Comment on the morphology of the erythrocytes.
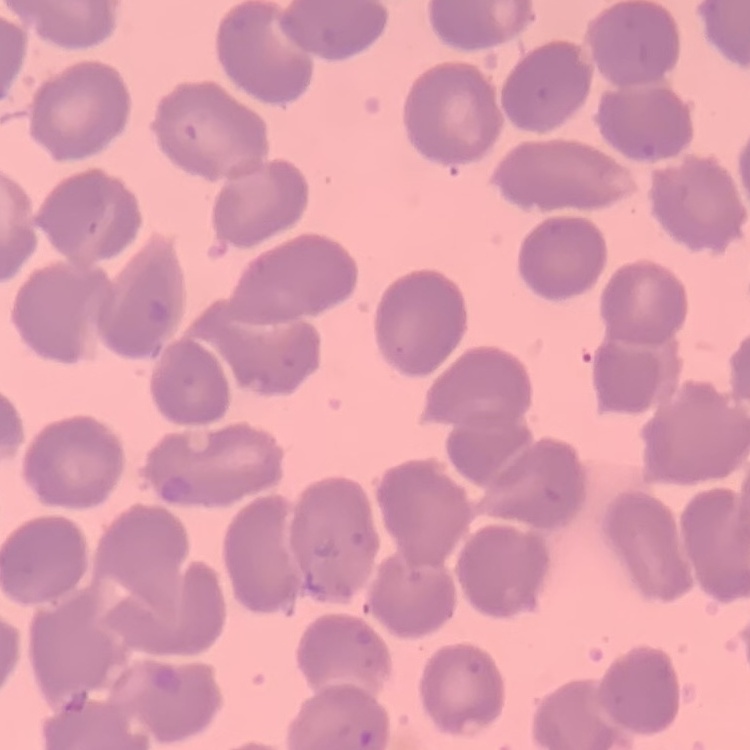
No rouleaux formation.

Summary:
  - Preparation: thin blood smear
  - Stain: Field's or Giemsa
  - Image type: one tile cut from a larger photomicrograph